Identify the parasite.
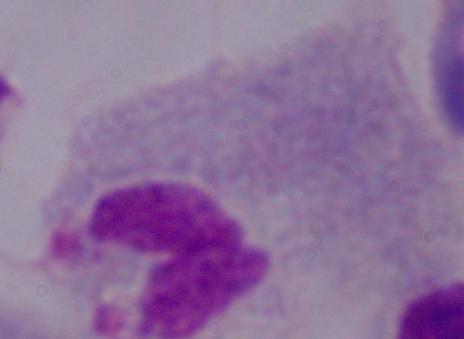
This is a trichomonad.

{
  "modality": "micrograph",
  "magnification": "1000x"
}